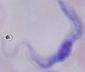
Micrograph. A trypanosome is shown. Captured at 1000x magnification.